Locate every blood parasite and identify its species.
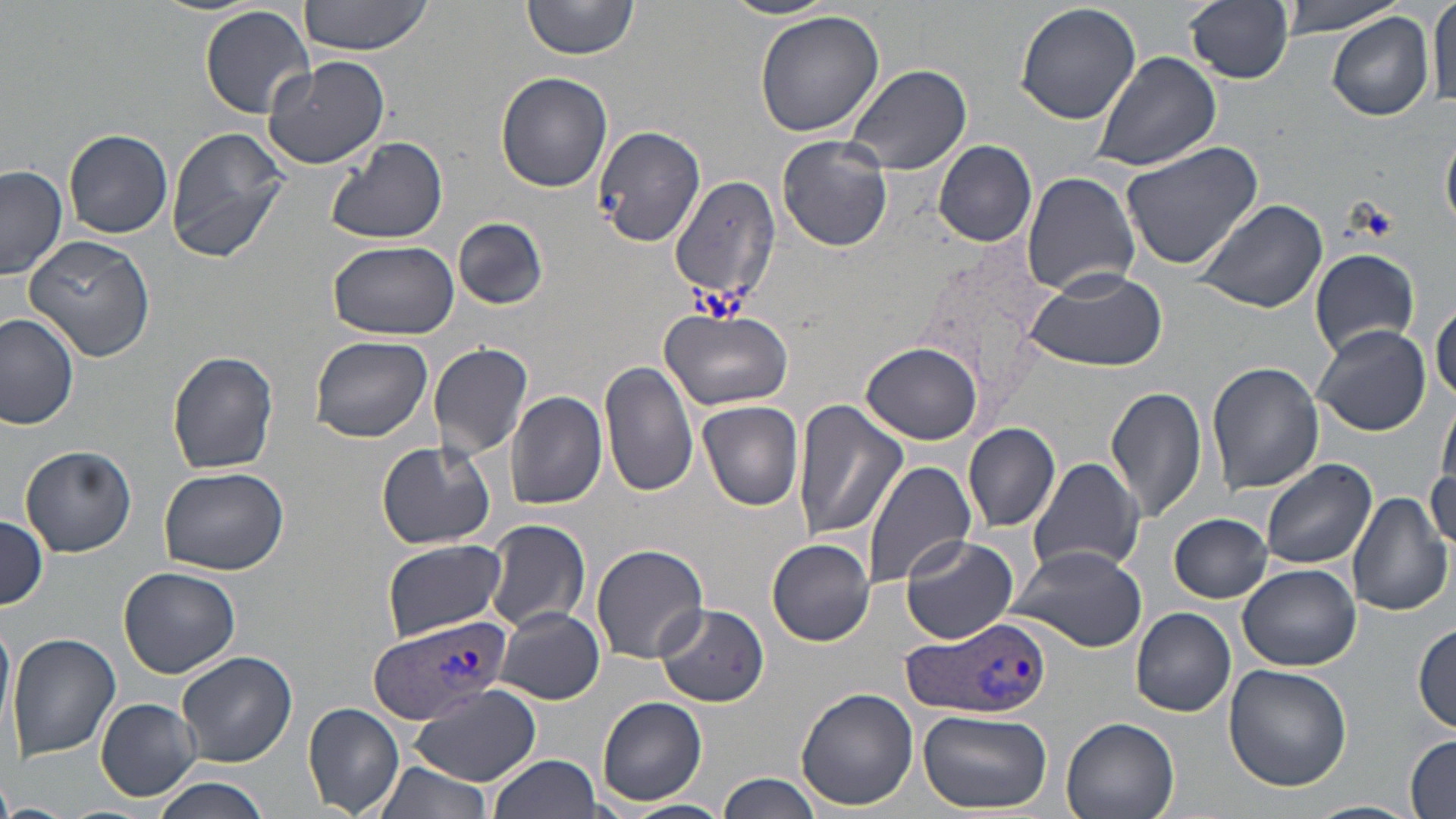
Approximate bounding boxes as (x1,y1)-(x2,y2) corner pairs in pixels.
Plasmodium vivax-infected red blood cells: (369,613)-(513,724), (898,614)-(1050,720).
No Plasmodium falciparum, Plasmodium ovale, Plasmodium malariae, Babesia divergens, or Trypanosoma brucei observed.

{
  "slide_level_diagnosis": "Plasmodium vivax",
  "platelet_locations": "approximate bounding boxes as (x1,y1)-(x2,y2) corner pairs in pixels: (687,283)-(750,318)",
  "image_size": "1456×819 pixels",
  "modality": "optical microscopy",
  "preparation": "thin blood smear",
  "uninfected_red_blood_cell_locations": "approximate bounding boxes as (x1,y1)-(x2,y2) corner pairs in pixels: (297,0)-(438,57), (521,0)-(641,60), (719,0)-(840,20), (1185,0)-(1295,84), (1276,0)-(1407,38), (1429,0)-(1455,110), (1015,3)-(1141,124), (199,4)-(317,117), (756,10)-(886,138), (1327,10)-(1436,123), (1092,50)-(1221,171), (260,57)-(392,170), (842,63)-(973,176), (496,71)-(612,193), (1442,123)-(1456,234), (163,126)-(290,262), (591,126)-(706,248), (63,129)-(173,237), (777,135)-(894,252), (324,136)-(449,246), (1118,138)-(1267,271), (934,140)-(1038,248), (1017,159)-(1255,285), (0,164)-(68,279), (1021,170)-(1141,296), (668,176)-(781,308), (1193,199)-(1328,314), (454,218)-(547,310), (21,231)-(158,360), (328,240)-(458,339), (1308,248)-(1421,357), (1021,267)-(1168,373), (1430,299)-(1456,403), (660,308)-(794,411), (0,314)-(79,429), (1313,323)-(1432,436), (311,336)-(433,441), (426,341)-(535,459), (862,342)-(983,445), (167,352)-(279,476), (600,359)-(699,498), (1207,361)-(1323,496), (500,384)-(602,625), (1106,386)-(1209,524), (506,391)-(608,511), (790,398)-(909,543), (697,401)-(805,510), (963,422)-(1061,533), (376,438)-(497,551), (1426,444)-(1456,561), (19,446)-(137,556), (1026,456)-(1146,578), (863,460)-(976,591), (1260,460)-(1376,570), (158,465)-(289,576), (1348,491)-(1452,617), (1169,513)-(1271,602), (0,516)-(47,611), (484,518)-(591,633), (900,535)-(1020,644), (381,539)-(505,639), (768,539)-(875,645), (591,544)-(709,662), (1005,545)-(1148,651), (1238,563)-(1360,672), (117,567)-(239,679), (655,604)-(769,707), (492,607)-(604,704), (1131,608)-(1236,717), (0,613)-(13,740), (1413,622)-(1455,736), (7,632)-(120,762), (177,651)-(297,766), (1222,662)-(1351,792), (412,686)-(541,785), (797,687)-(919,809), (597,695)-(709,806), (95,698)-(202,799), (302,703)-(405,816), (918,709)-(1052,814), (1062,716)-(1181,819), (1406,735)-(1456,817), (489,754)-(602,819), (370,757)-(496,819), (718,773)-(826,819), (152,778)-(271,819), (623,799)-(731,819), (1307,799)-(1423,819)",
  "stain": "May-Grünwald-Giemsa",
  "magnification": "1000x",
  "field_of_view": "single"
}